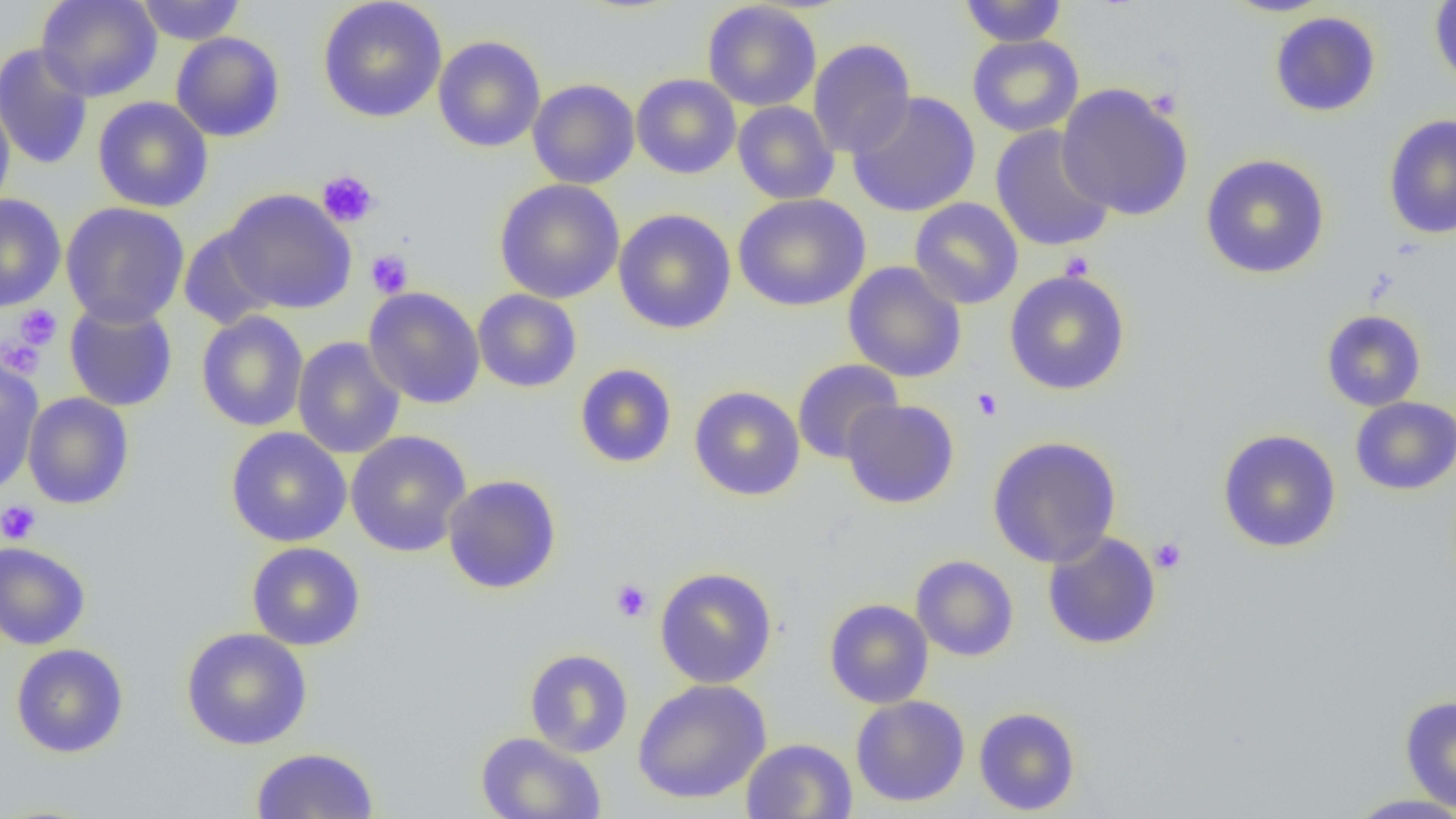 Approximate bounding boxes as [x1, y1, x2, y2] in pixels. Platelet locations: [317, 170, 379, 228], [366, 249, 414, 298], [1060, 252, 1094, 281], [14, 305, 62, 350], [2, 337, 46, 379], [971, 388, 1003, 421], [0, 500, 41, 544], [1150, 537, 1188, 574], [610, 578, 652, 622]. Uninfected red blood cell locations: [35, 0, 162, 102], [136, 0, 246, 45], [317, 0, 447, 123], [959, 0, 1067, 47], [1221, 0, 1334, 17], [1429, 0, 1456, 91], [702, 1, 821, 111], [1269, 11, 1381, 117], [170, 32, 285, 142], [967, 34, 1084, 137], [432, 35, 546, 152], [808, 39, 916, 159], [0, 43, 95, 170], [631, 74, 741, 179], [527, 79, 640, 189], [1057, 83, 1194, 221], [847, 91, 980, 217], [0, 93, 15, 215], [92, 96, 213, 212], [732, 101, 839, 205], [1383, 114, 1456, 240], [990, 125, 1115, 253], [1200, 154, 1330, 279], [494, 179, 625, 304], [220, 188, 358, 314], [732, 193, 871, 312], [0, 194, 66, 311], [909, 197, 1024, 309], [60, 202, 190, 328], [613, 209, 737, 334], [179, 225, 280, 331], [843, 262, 967, 382], [1004, 269, 1131, 395], [363, 287, 485, 409], [472, 289, 582, 393], [63, 299, 178, 412], [1321, 310, 1427, 411], [195, 311, 309, 432], [292, 337, 406, 459], [0, 356, 44, 495], [791, 359, 904, 464], [574, 363, 677, 469], [689, 385, 805, 501], [22, 392, 134, 509], [1350, 396, 1456, 495], [841, 399, 959, 509], [225, 427, 352, 547], [1216, 429, 1342, 553], [345, 430, 472, 557], [987, 436, 1122, 568], [442, 474, 562, 594], [1042, 531, 1162, 650], [0, 541, 91, 650], [246, 541, 365, 651], [911, 555, 1019, 661], [653, 566, 778, 689], [823, 598, 934, 709], [181, 627, 313, 750], [11, 643, 129, 758], [524, 649, 633, 758], [632, 679, 772, 804], [1399, 694, 1456, 812], [850, 696, 970, 807], [974, 707, 1080, 815], [475, 732, 606, 819], [741, 738, 857, 818], [250, 747, 380, 818], [1345, 794, 1456, 818]. Slide-level diagnosis: no evidence of blood parasites. Single field of view. 1000x magnification. Image is 1456×819 pixels. Thin blood film. Light microscopy.